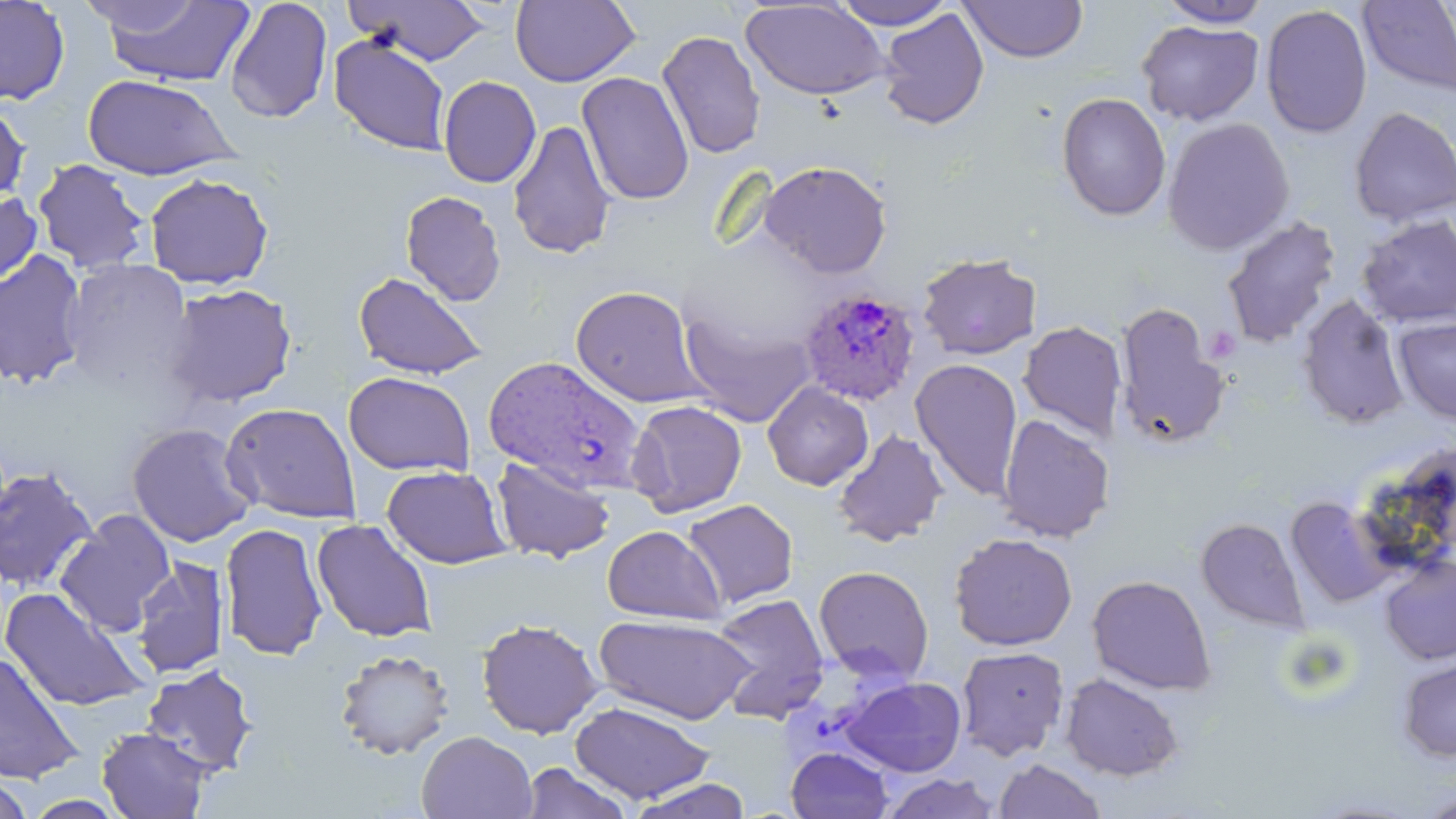
Approximate bounding boxes as [x1, y1, x2, y2] in pixels. Plasmodium ovale-infected red blood cell locations: [799, 287, 919, 404], [484, 354, 655, 491]. Uninfected red blood cell locations: [96, 0, 255, 87], [224, 0, 333, 123], [343, 0, 492, 66], [830, 0, 956, 30], [1155, 0, 1274, 28], [0, 1, 70, 106], [510, 1, 640, 87], [741, 1, 891, 101], [959, 1, 1088, 64], [1358, 1, 1456, 98], [1260, 5, 1372, 139], [877, 8, 989, 130], [1136, 19, 1264, 127], [656, 30, 767, 159], [328, 32, 451, 156], [576, 71, 694, 206], [82, 74, 238, 180], [438, 76, 541, 188], [1056, 92, 1171, 222], [0, 98, 31, 207], [1349, 107, 1456, 227], [1161, 117, 1294, 256], [507, 118, 616, 260], [32, 158, 151, 275], [758, 159, 893, 278], [144, 173, 274, 290], [0, 189, 42, 290], [400, 190, 506, 306], [1356, 214, 1456, 327], [1221, 216, 1341, 349], [0, 250, 89, 389], [916, 252, 1042, 360], [59, 258, 195, 393], [352, 270, 488, 380], [163, 283, 298, 408], [569, 285, 709, 409], [1296, 294, 1410, 431], [678, 305, 818, 428], [1114, 305, 1229, 448], [1392, 316, 1456, 426], [1018, 321, 1127, 441], [910, 359, 1024, 501], [343, 371, 475, 477], [762, 382, 874, 491], [626, 399, 747, 517], [220, 402, 361, 524], [997, 413, 1116, 542], [126, 422, 257, 547], [832, 429, 948, 547], [490, 456, 616, 564], [382, 465, 512, 569], [0, 466, 98, 594], [1286, 496, 1399, 607], [681, 499, 799, 609], [55, 509, 176, 636], [1195, 517, 1308, 632], [311, 518, 437, 643], [219, 522, 328, 661], [602, 525, 726, 624], [948, 532, 1078, 652], [1379, 555, 1456, 665], [130, 557, 230, 680], [813, 565, 934, 685], [1086, 574, 1216, 694], [0, 587, 152, 713], [708, 592, 830, 723], [593, 614, 755, 725], [475, 618, 604, 739], [955, 645, 1070, 761], [334, 648, 456, 761], [0, 652, 84, 784], [1397, 656, 1456, 762], [140, 664, 258, 777], [1059, 672, 1184, 781], [841, 676, 967, 777], [569, 700, 714, 804], [96, 727, 212, 818], [416, 731, 538, 819], [785, 747, 893, 819], [994, 759, 1107, 818], [519, 762, 634, 819], [0, 772, 35, 819], [879, 772, 1002, 818], [624, 778, 755, 818], [1417, 791, 1456, 819]. Slide-level diagnosis: Plasmodium ovale. May-Grünwald-Giemsa stain. Thin blood film. Optical microscopy. 1000x magnification. Single field of view. Image is 1456×819 pixels.